Outline each Trypanosoma brucei.
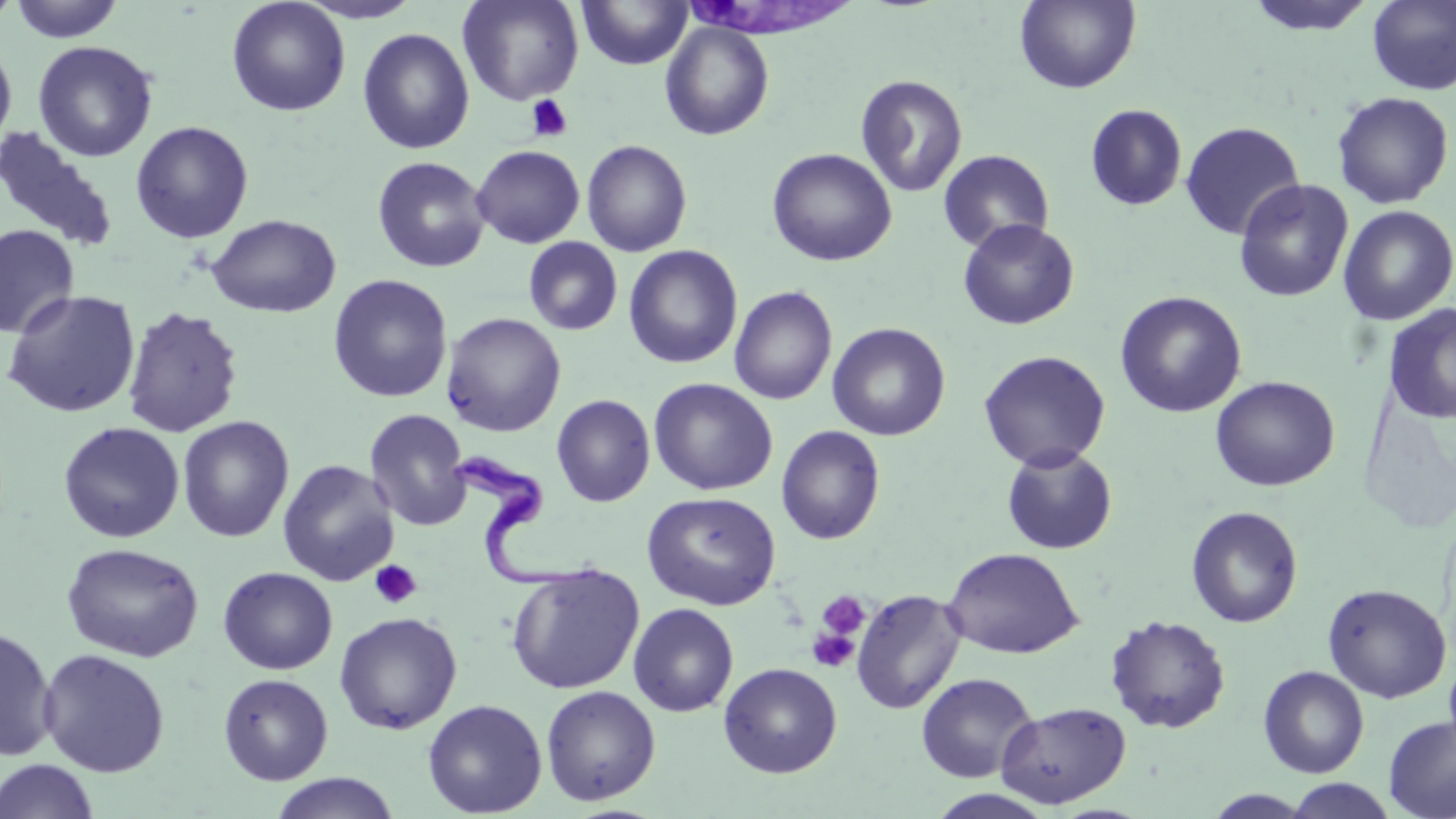
Approximate bounding boxes as (x1, y1, x2, y2) in pixels.
Trypanosoma brucei: (448, 449, 589, 593).

Uninfected red blood cell locations: (0, 0, 21, 27), (9, 0, 124, 43), (297, 0, 424, 24), (457, 0, 584, 106), (577, 0, 693, 70), (1015, 0, 1141, 93), (1244, 0, 1377, 36), (1367, 0, 1456, 95), (226, 1, 350, 116), (660, 22, 774, 141), (357, 27, 474, 155), (0, 39, 17, 153), (32, 40, 158, 162), (855, 74, 968, 197), (1331, 91, 1454, 209), (1085, 103, 1188, 211), (130, 120, 254, 243), (1179, 121, 1305, 240), (0, 127, 119, 253), (581, 140, 692, 257), (471, 145, 585, 248), (766, 147, 897, 267), (938, 149, 1055, 253), (372, 155, 490, 273), (1233, 178, 1354, 303), (1337, 205, 1456, 326), (206, 214, 341, 318), (956, 219, 1080, 330), (0, 225, 78, 339), (523, 237, 623, 335), (624, 245, 743, 369), (328, 273, 453, 403), (729, 285, 837, 405), (2, 288, 141, 418), (1114, 290, 1247, 418), (1384, 303, 1456, 425), (121, 305, 244, 438), (441, 312, 566, 437), (827, 322, 950, 441), (978, 350, 1111, 472), (1210, 375, 1340, 492), (648, 378, 778, 496), (552, 393, 655, 507), (364, 408, 473, 532), (177, 416, 294, 543), (58, 422, 185, 543), (776, 425, 885, 545), (1001, 445, 1118, 555), (278, 459, 399, 586), (642, 491, 781, 610), (1186, 506, 1303, 628), (61, 542, 203, 662), (943, 546, 1084, 658), (506, 563, 645, 694), (218, 566, 338, 674), (1322, 583, 1452, 703), (851, 588, 965, 715), (628, 602, 739, 717), (334, 611, 462, 735), (1105, 614, 1231, 734), (0, 626, 58, 761), (37, 648, 170, 778), (1444, 650, 1456, 762), (719, 662, 842, 778), (1258, 665, 1369, 778), (916, 672, 1039, 783), (218, 673, 333, 785), (541, 684, 661, 806), (422, 698, 548, 817), (996, 701, 1131, 808), (1384, 716, 1456, 819), (1, 758, 99, 819), (270, 772, 400, 819), (1285, 779, 1398, 818), (1203, 789, 1319, 818). Platelet locations: (526, 94, 573, 143), (370, 559, 422, 609), (816, 590, 870, 640), (806, 628, 859, 673). Slide-level diagnosis: Trypanosoma brucei. May-Grünwald-Giemsa stain. Single field of view. Thin blood smear. 1000x magnification. Optical microscopy. Image is 1456×819 pixels.